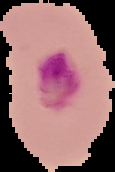 Image is 115×172 pixels. From a thin blood smear. Segmented cell region on a black background. Result: Plasmodium parasites identified.